Locate every Plasmodium parasite.
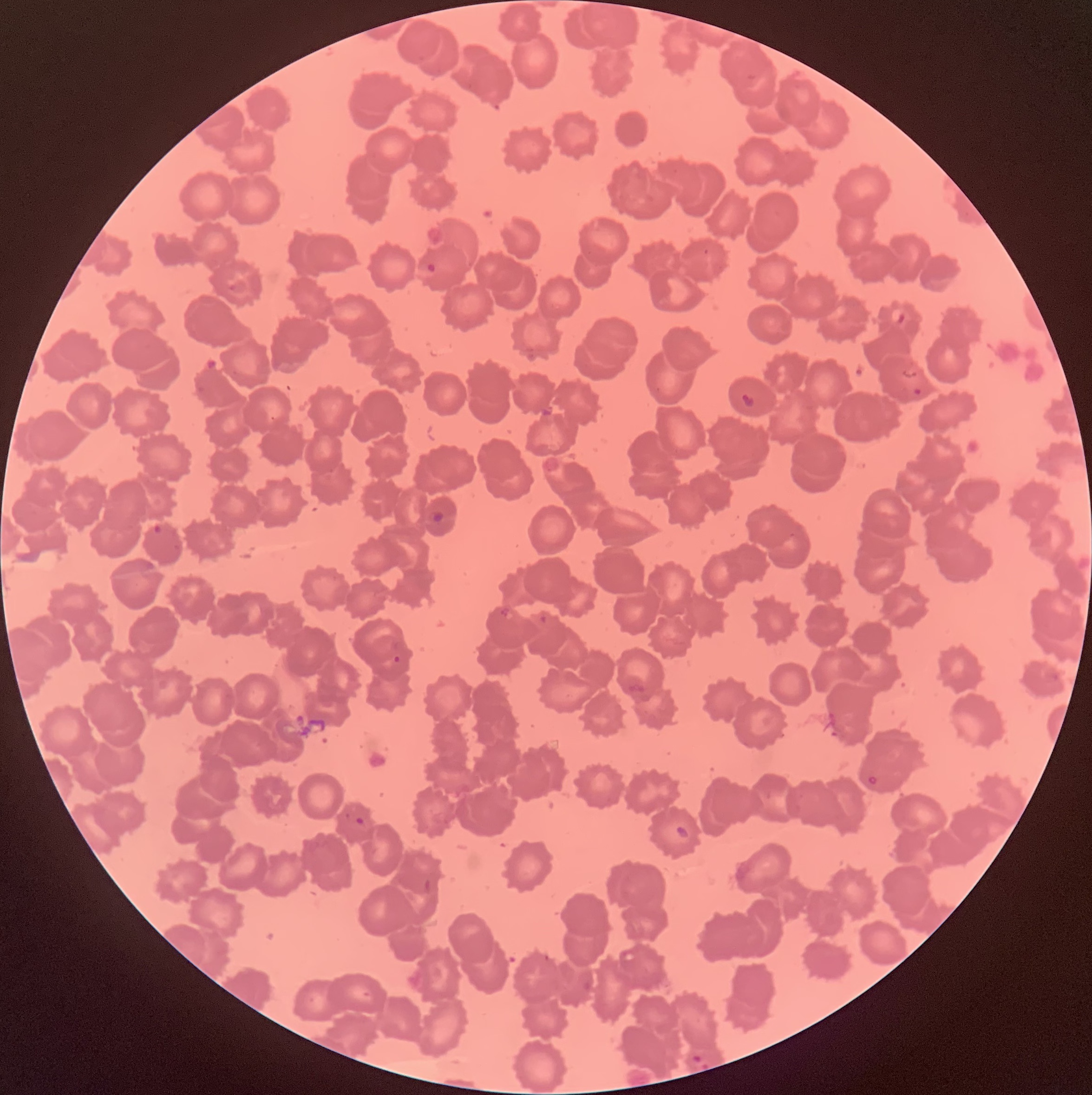

Approximate bounding boxes as (x1, y1, x2, y2) in pixels.
Plasmodium parasites: (427, 262, 436, 274), (892, 308, 907, 325), (913, 388, 922, 396), (740, 393, 755, 409), (428, 510, 444, 523), (153, 523, 164, 536), (498, 607, 511, 618), (539, 614, 548, 624), (392, 655, 401, 663), (867, 775, 878, 785), (355, 815, 365, 825), (675, 826, 691, 840), (691, 1054, 703, 1064).

Optical microscopy. Thin blood film. Image is 1092×1095 pixels. The red blood cells show rouleaux formation.